Classify this cell by malaria status.
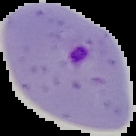
It is parasitized.

Summary:
  - Image size: 136×136 pixels
  - Preparation: thin blood film
  - Image type: segmented cell region with the area outside set to black